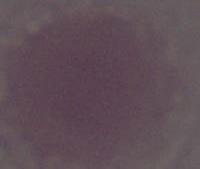

An erythrocyte is seen. Captured at 1000x magnification. Photomicrograph.